Name the parasite shown.
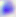
This is Toxoplasma gondii.

Micrograph. 400x magnification.